Report the malaria status of this cell.
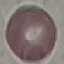

It is uninfected.

Thin blood smear. Giemsa stain. Cell patch, automatically extracted from a larger field of view and resized to 64 × 64 pixels. Acquired by smartphone through the microscope eyepiece.